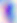 Micrograph. Toxoplasma gondii is seen. Captured at 400x magnification.